Identify the cell.
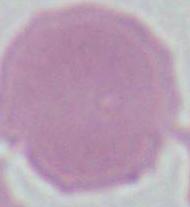
An erythrocyte.

Summary:
  - Magnification: 1000x
  - Modality: micrograph